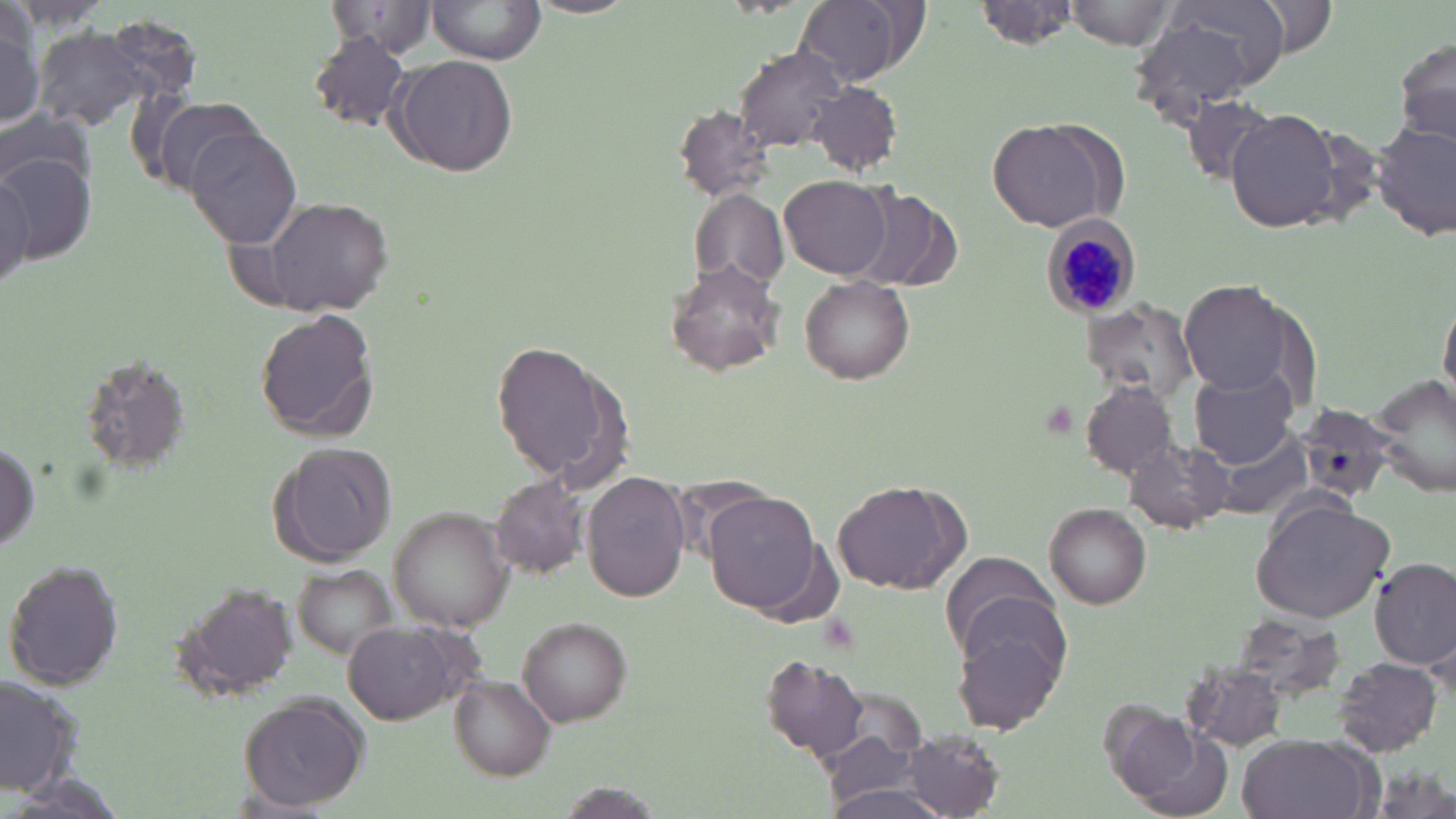
Summary:
  - Coordinate format: approximate bounding boxes as (x1, y1, x2, y2) in pixels
  - Plasmodium malariae-infected red blood cell locations: (1047, 219, 1140, 319)
  - Uninfected red blood cell locations: (794, 0, 921, 87), (979, 0, 1080, 51), (1065, 0, 1178, 51), (1167, 0, 1291, 79), (1254, 0, 1338, 58), (426, 1, 545, 68), (326, 2, 438, 57), (1129, 13, 1261, 126), (0, 21, 44, 127), (28, 27, 164, 135), (308, 33, 414, 131), (1395, 36, 1456, 148), (736, 44, 846, 152), (390, 56, 517, 177), (808, 80, 903, 177), (1185, 95, 1282, 182), (151, 96, 261, 196), (676, 107, 776, 201), (1227, 109, 1342, 232), (987, 118, 1122, 232), (1373, 121, 1455, 238), (186, 126, 304, 250), (0, 154, 97, 263), (0, 168, 33, 296), (779, 175, 893, 278), (849, 188, 954, 291), (690, 189, 790, 286), (267, 199, 393, 316), (665, 261, 785, 375), (800, 278, 916, 384), (1179, 280, 1289, 393), (1441, 298, 1456, 403), (1084, 303, 1198, 397), (258, 311, 379, 443), (493, 341, 620, 484), (79, 357, 193, 479), (1191, 368, 1302, 468), (1370, 375, 1456, 501), (1080, 381, 1179, 478), (1293, 402, 1403, 502), (0, 433, 41, 561), (1212, 434, 1312, 521), (1126, 438, 1233, 535), (272, 443, 401, 567), (583, 471, 693, 603), (491, 475, 589, 580), (832, 478, 969, 594), (703, 492, 824, 612), (1251, 497, 1395, 624), (1045, 503, 1150, 607), (391, 507, 510, 628), (939, 550, 1068, 667), (1371, 558, 1455, 670), (5, 560, 125, 691), (292, 563, 395, 659), (170, 580, 297, 696), (519, 616, 632, 726), (953, 616, 1069, 736), (341, 623, 467, 724), (760, 654, 872, 762), (1331, 656, 1446, 759), (1182, 665, 1293, 754), (450, 676, 555, 779), (0, 677, 86, 798), (238, 693, 370, 810), (1106, 711, 1229, 816), (902, 732, 1003, 816), (1237, 733, 1375, 819)
  - Slide-level diagnosis: Plasmodium malariae
  - Image size: 1456×819 pixels
  - Magnification: 1000x
  - Modality: light microscopy
  - Field of view: one of a larger specimen
  - Preparation: thin blood smear
  - Stain: May-Grünwald-Giemsa